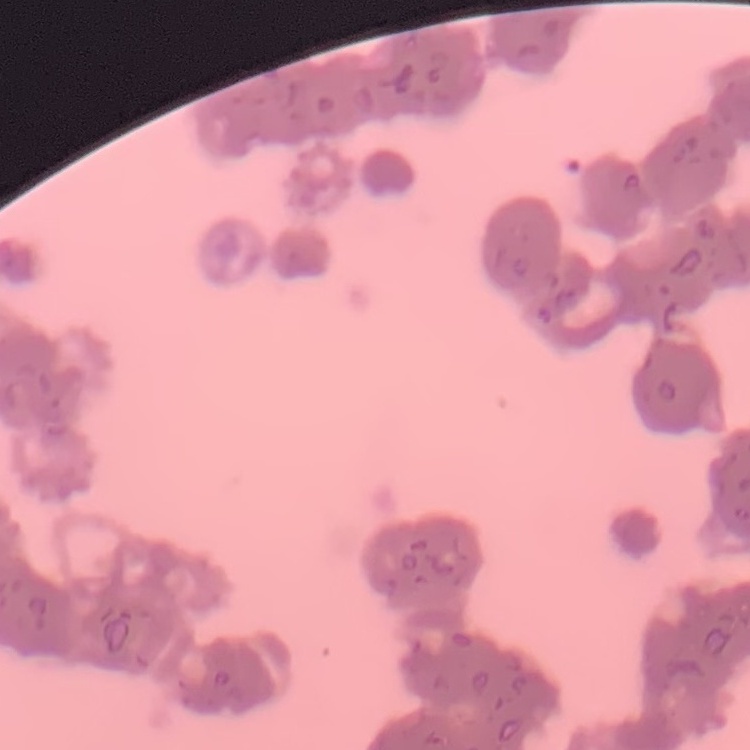

erythrocyte morphology = rouleaux formation
image type = square crop of a larger photomicrograph
stain = Field's or Giemsa
preparation = thin peripheral smear